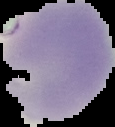

preparation = thin blood film
result = negative for Plasmodium parasites
image size = 115×127 pixels
image type = segmented cell region with the area outside set to black